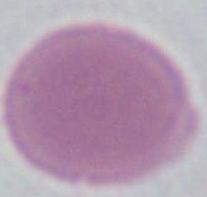

identification = red blood cell
magnification = 1000x
modality = micrograph